Report the malaria status of this cell.
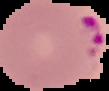

It is parasitized.

Image is 109×91 pixels. From a thin blood smear. The area outside the segmented cell region is set to black.